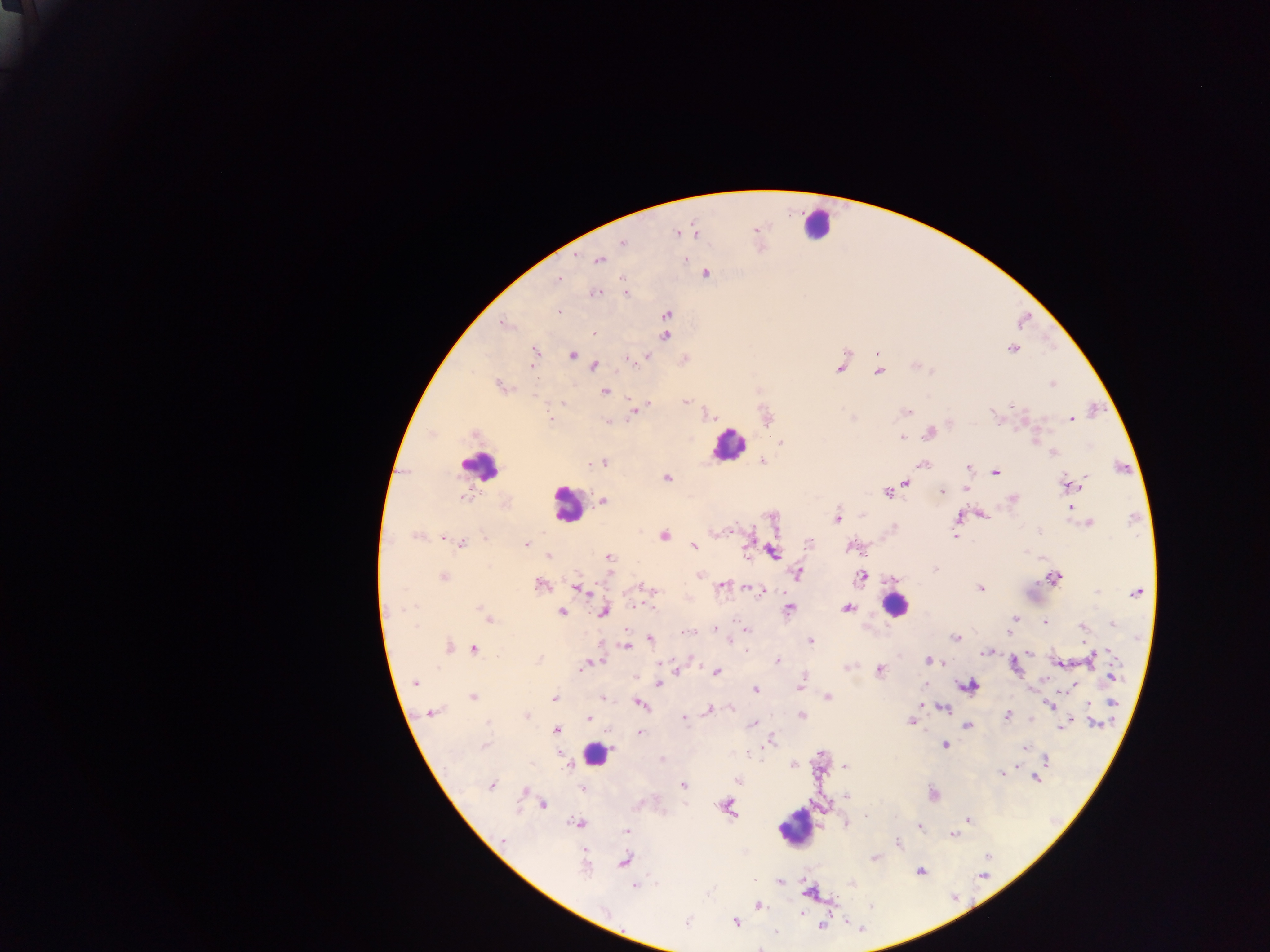

image size = 1270×952 pixels
field of view = single
country = Ghana
leukocyte locations = approximate centers as (x, y) in pixels: (814, 224), (728, 444), (480, 466), (567, 504), (894, 604), (596, 753), (795, 827)
preparation = thick blood smear
Plasmodium parasite locations = approximate centers as (x, y) in pixels: (756, 229), (677, 232), (694, 232), (622, 242), (685, 258), (599, 260), (704, 272), (557, 279), (595, 292), (625, 293), (558, 312), (667, 315), (503, 323), (593, 333), (664, 335), (1011, 348), (535, 352), (877, 353), (573, 354), (645, 356), (628, 359), (684, 359), (593, 365), (840, 367), (878, 370), (1051, 384), (501, 386), (604, 391), (686, 401), (635, 409), (905, 411), (765, 417), (852, 417), (550, 419), (1071, 419), (607, 422), (929, 431), (901, 437), (780, 442), (1053, 453), (602, 462), (761, 462), (920, 464), (967, 467), (995, 472), (667, 478), (903, 482), (1069, 484), (965, 487), (887, 491), (940, 492), (1012, 498), (602, 501), (1070, 507), (982, 513), (957, 517), (836, 519), (1088, 522), (892, 528), (416, 535), (662, 535), (955, 535), (442, 536), (461, 542), (525, 543), (809, 543), (693, 546), (852, 546), (773, 552), (549, 556), (608, 557), (934, 569), (700, 573), (798, 573), (442, 575), (861, 575), (1053, 577), (891, 580), (541, 584), (721, 586), (642, 587), (747, 587), (578, 588), (979, 589), (761, 590), (1137, 590), (846, 607), (788, 609), (561, 611), (602, 611), (1014, 618), (488, 619), (1043, 622), (1011, 623), (1113, 624), (1083, 627), (745, 628), (716, 630), (1010, 630), (690, 631), (730, 638), (957, 638), (650, 639), (810, 641), (626, 645), (447, 648), (474, 649), (985, 651), (1029, 652), (777, 660), (928, 660), (1089, 660), (1058, 662), (589, 663), (1013, 665), (583, 666), (847, 667), (677, 669), (879, 670), (716, 671), (1110, 676), (414, 682), (658, 683), (968, 685), (799, 686), (1074, 687), (755, 689), (472, 697), (555, 697), (827, 697), (1094, 701), (638, 703), (1090, 704), (1050, 705), (942, 707), (730, 708), (708, 710), (431, 713), (1008, 715), (526, 716), (802, 716), (589, 718), (683, 718), (1029, 719), (912, 721), (1094, 723), (752, 724), (967, 725), (1060, 726), (556, 730), (640, 733), (771, 741), (945, 744), (1025, 747), (662, 759), (1044, 759), (566, 763), (793, 765), (845, 767), (1001, 773), (1037, 777), (738, 780), (491, 785), (683, 786), (581, 787), (526, 791), (933, 795), (845, 797), (541, 804), (725, 806), (865, 815), (967, 820), (578, 823), (844, 823), (918, 826), (627, 831), (953, 835), (898, 844), (875, 857), (624, 860), (919, 870), (779, 881), (851, 884), (635, 885), (757, 906), (735, 921), (820, 924)
capture = mobile-phone photograph through a microscope